Locate every Plasmodium parasite.
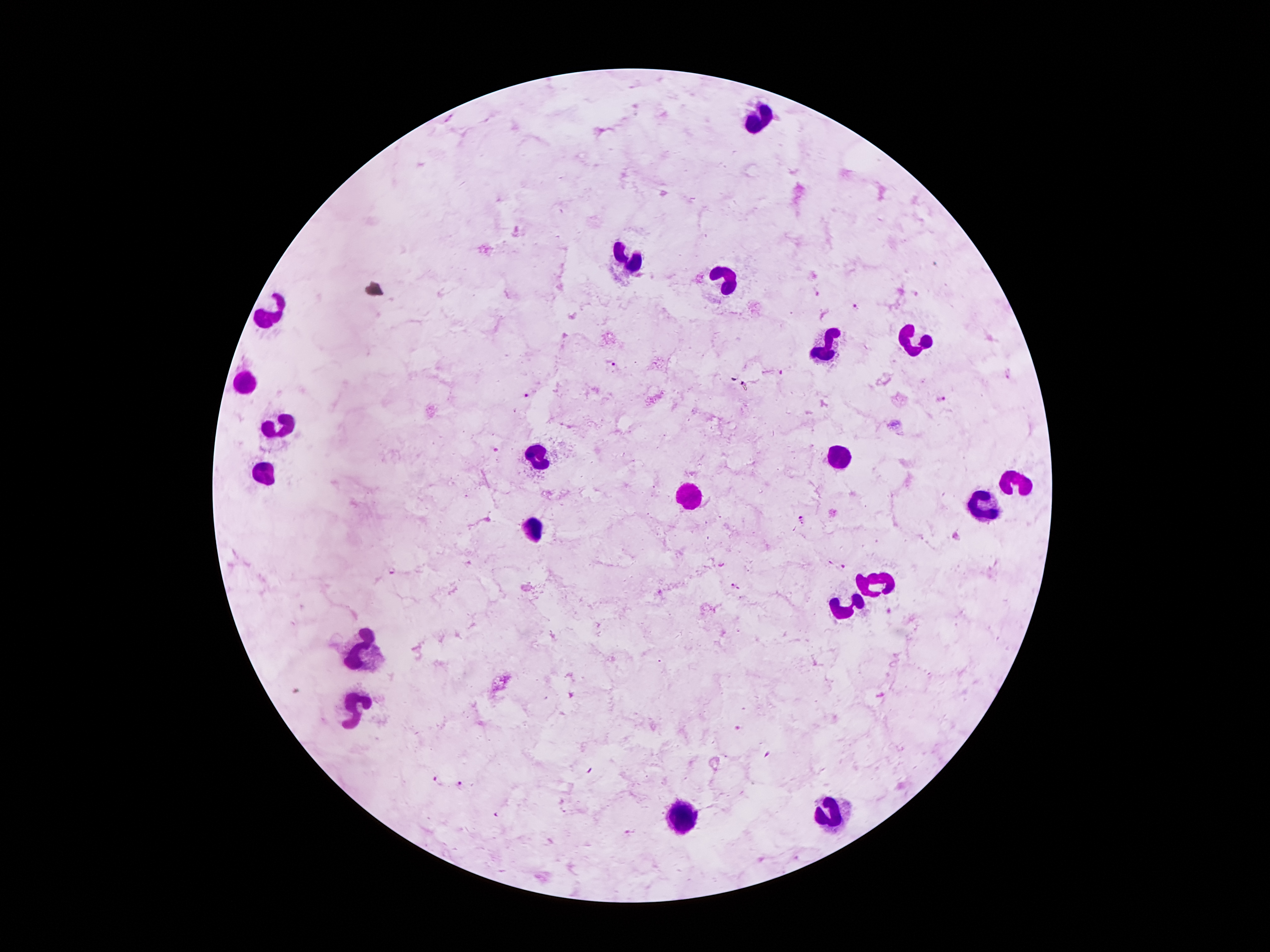

Approximate centers as {x, y} in pixels.
Plasmodium parasites: {817, 294}, {856, 306}, {609, 362}, {780, 372}, {527, 395}, {941, 399}, {495, 447}, {804, 520}, {956, 537}, {392, 571}, {734, 586}, {739, 727}, {768, 754}, {439, 780}, {459, 786}, {497, 814}, {628, 830}.

Summary:
  - Leukocyte locations: {763, 115}, {628, 260}, {726, 279}, {275, 312}, {914, 339}, {832, 348}, {244, 385}, {285, 423}, {535, 455}, {845, 459}, {265, 477}, {1013, 480}, {688, 497}, {985, 506}, {532, 528}, {878, 582}, {842, 612}, {367, 646}, {357, 711}, {833, 814}, {684, 816}
  - Preparation: thick blood film
  - Stain: Giemsa
  - Patient malaria status: positive for Plasmodium falciparum
  - Field of view: one from this slide
  - Image size: 1270×952 pixels
  - Magnification: 100x
  - Capture: smartphone camera through the microscope eyepiece